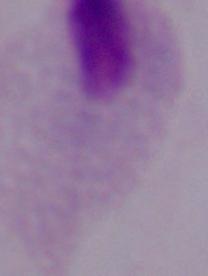

1000x magnification. A trichomonad is seen. Micrograph.